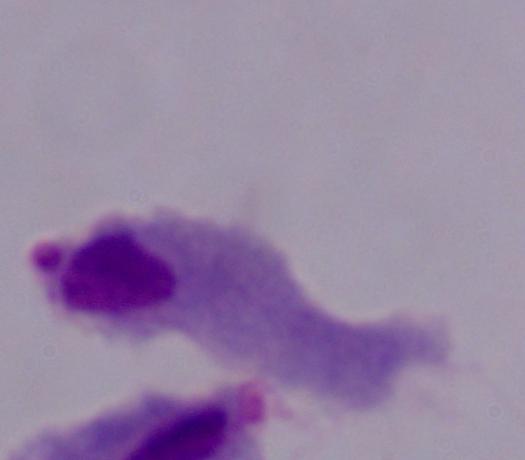

Summary:
  - Magnification: 1000x
  - Identification: trichomonad
  - Modality: micrograph